Outline each Plasmodium falciparum-infected red blood cell.
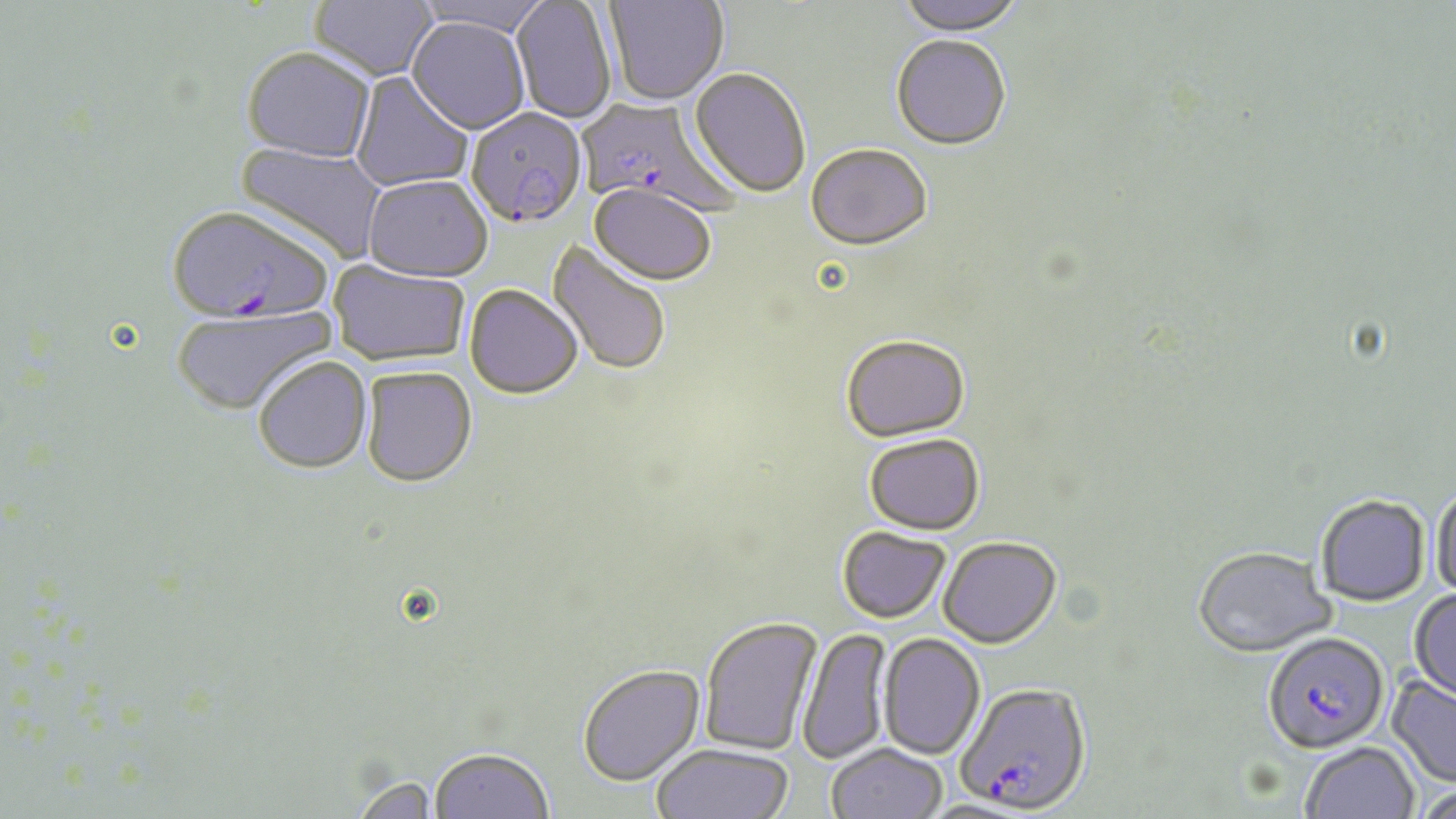
Approximate bounding boxes as [x1, y1, x2, y2] in pixels.
Plasmodium falciparum-infected red blood cells: [575, 96, 739, 218], [466, 108, 588, 229], [166, 206, 333, 328], [1263, 631, 1389, 753], [957, 682, 1091, 813].

Summary:
  - Uninfected red blood cell locations: [309, 0, 438, 82], [412, 0, 555, 37], [604, 0, 728, 105], [895, 0, 1026, 35], [511, 1, 617, 125], [406, 17, 531, 135], [890, 34, 1011, 149], [241, 47, 377, 163], [689, 67, 811, 198], [350, 72, 475, 192], [235, 141, 388, 265], [806, 142, 933, 250], [363, 175, 493, 282], [587, 184, 718, 286], [547, 240, 672, 378], [329, 260, 471, 367], [464, 285, 583, 400], [172, 307, 335, 418], [841, 333, 970, 441], [254, 357, 373, 474], [360, 366, 477, 488], [863, 433, 985, 533], [1430, 484, 1456, 601], [1315, 494, 1430, 605], [837, 525, 951, 622], [938, 535, 1062, 648], [1193, 545, 1335, 657], [1410, 589, 1456, 701], [699, 615, 823, 756], [797, 627, 892, 765], [878, 633, 985, 760], [577, 663, 705, 786], [1387, 675, 1456, 788], [1300, 741, 1420, 819], [651, 743, 794, 819], [825, 743, 947, 819], [429, 749, 554, 819], [1412, 785, 1456, 819]
  - Slide-level diagnosis: Plasmodium falciparum
  - Field of view: one of a larger specimen
  - Modality: light microscopy
  - Image size: 1456×819 pixels
  - Magnification: 1000x
  - Preparation: thin blood film
  - Stain: May-Grünwald-Giemsa